Outline each blood parasite and name the species.
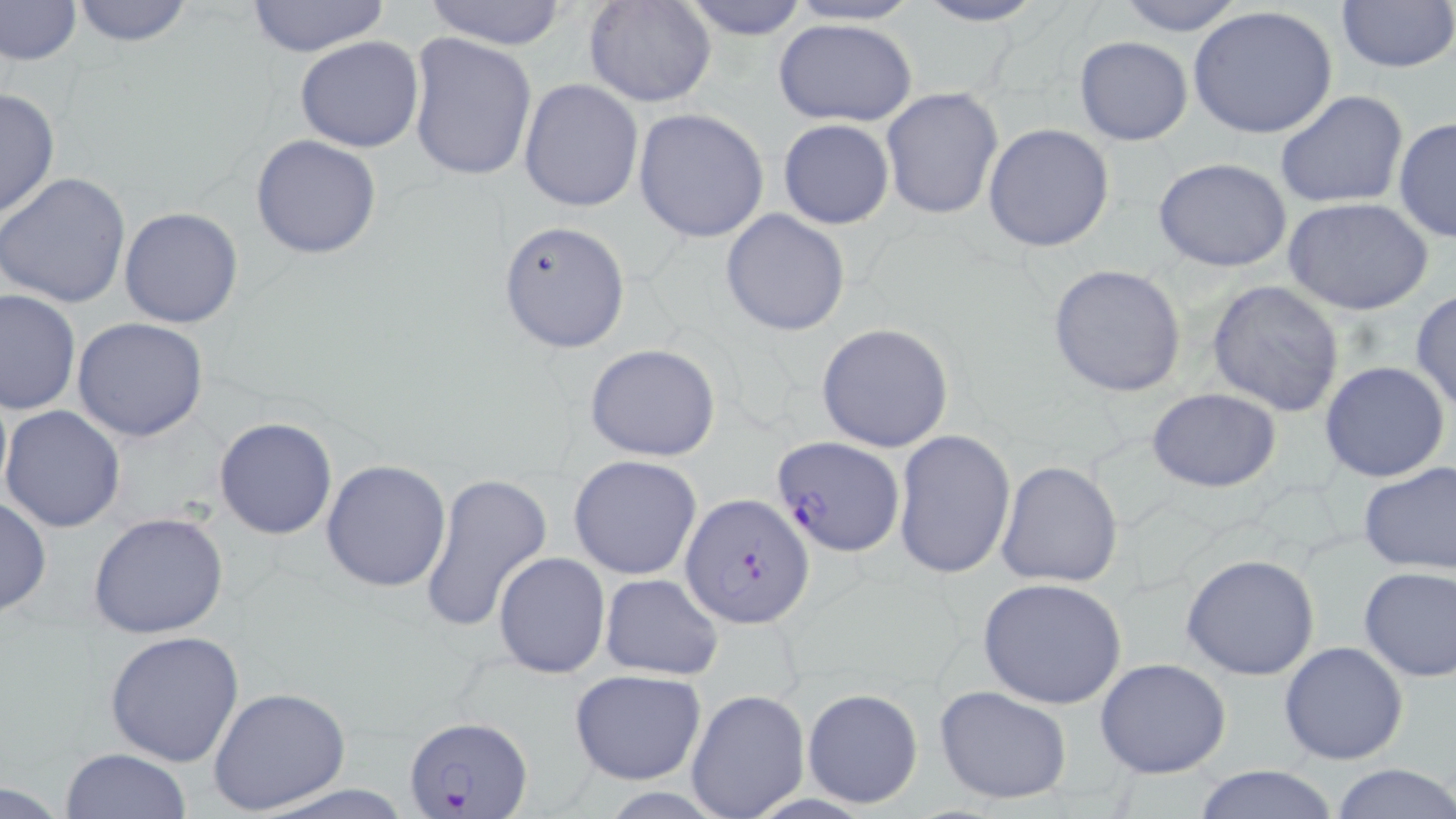
Approximate bounding boxes as named x1/y1/x2/y2 corners in pixels.
Plasmodium falciparum-infected red blood cells: (x1=770, y1=433, x2=904, y2=559), (x1=681, y1=494, x2=813, y2=629), (x1=402, y1=712, x2=534, y2=817).
No Plasmodium ovale, Plasmodium malariae, Plasmodium vivax, Babesia divergens, or Trypanosoma brucei observed.

Summary:
  - Uninfected red blood cell locations: (x1=0, y1=0, x2=82, y2=68), (x1=584, y1=0, x2=716, y2=107), (x1=679, y1=0, x2=811, y2=41), (x1=784, y1=0, x2=925, y2=26), (x1=912, y1=0, x2=1050, y2=27), (x1=1113, y1=0, x2=1249, y2=36), (x1=68, y1=1, x2=196, y2=48), (x1=242, y1=1, x2=393, y2=58), (x1=421, y1=1, x2=572, y2=49), (x1=1334, y1=1, x2=1455, y2=75), (x1=1188, y1=6, x2=1339, y2=142), (x1=772, y1=17, x2=918, y2=127), (x1=406, y1=32, x2=536, y2=184), (x1=295, y1=36, x2=425, y2=154), (x1=1073, y1=36, x2=1194, y2=147), (x1=518, y1=78, x2=643, y2=213), (x1=0, y1=86, x2=59, y2=220), (x1=880, y1=87, x2=1004, y2=220), (x1=1275, y1=89, x2=1408, y2=210), (x1=633, y1=109, x2=769, y2=243), (x1=1393, y1=118, x2=1455, y2=243), (x1=778, y1=119, x2=894, y2=230), (x1=983, y1=123, x2=1114, y2=252), (x1=250, y1=135, x2=381, y2=260), (x1=1152, y1=158, x2=1294, y2=272), (x1=0, y1=172, x2=131, y2=308), (x1=1285, y1=199, x2=1433, y2=316), (x1=119, y1=206, x2=245, y2=329), (x1=721, y1=208, x2=852, y2=336), (x1=498, y1=219, x2=629, y2=352), (x1=1047, y1=264, x2=1187, y2=398), (x1=1206, y1=279, x2=1346, y2=416), (x1=0, y1=288, x2=80, y2=416), (x1=1410, y1=289, x2=1456, y2=412), (x1=72, y1=317, x2=208, y2=442), (x1=815, y1=322, x2=954, y2=452), (x1=584, y1=344, x2=722, y2=462), (x1=1319, y1=361, x2=1451, y2=484), (x1=1145, y1=387, x2=1282, y2=493), (x1=1, y1=406, x2=126, y2=532), (x1=213, y1=417, x2=338, y2=540), (x1=893, y1=430, x2=1016, y2=581), (x1=568, y1=456, x2=702, y2=579), (x1=321, y1=458, x2=452, y2=592), (x1=996, y1=460, x2=1124, y2=589), (x1=1357, y1=463, x2=1456, y2=575), (x1=418, y1=473, x2=551, y2=634), (x1=0, y1=495, x2=50, y2=617), (x1=88, y1=512, x2=230, y2=640), (x1=493, y1=552, x2=611, y2=679), (x1=1181, y1=554, x2=1320, y2=681), (x1=1358, y1=565, x2=1456, y2=681), (x1=599, y1=573, x2=723, y2=679), (x1=977, y1=578, x2=1128, y2=709), (x1=104, y1=628, x2=245, y2=766), (x1=1278, y1=641, x2=1409, y2=767), (x1=1095, y1=658, x2=1231, y2=779), (x1=568, y1=670, x2=707, y2=785), (x1=933, y1=685, x2=1074, y2=803), (x1=208, y1=687, x2=351, y2=815), (x1=801, y1=688, x2=921, y2=809), (x1=686, y1=689, x2=810, y2=819), (x1=62, y1=748, x2=191, y2=819), (x1=1332, y1=762, x2=1456, y2=819), (x1=1186, y1=765, x2=1342, y2=819), (x1=0, y1=778, x2=70, y2=816)
  - Slide-level diagnosis: Plasmodium falciparum
  - Stain: May-Grünwald-Giemsa
  - Modality: optical microscopy
  - Image size: 1456×819 pixels
  - Magnification: 1000x
  - Preparation: thin blood film
  - Field of view: one of a larger specimen